Assess the morphology of the erythrocytes.
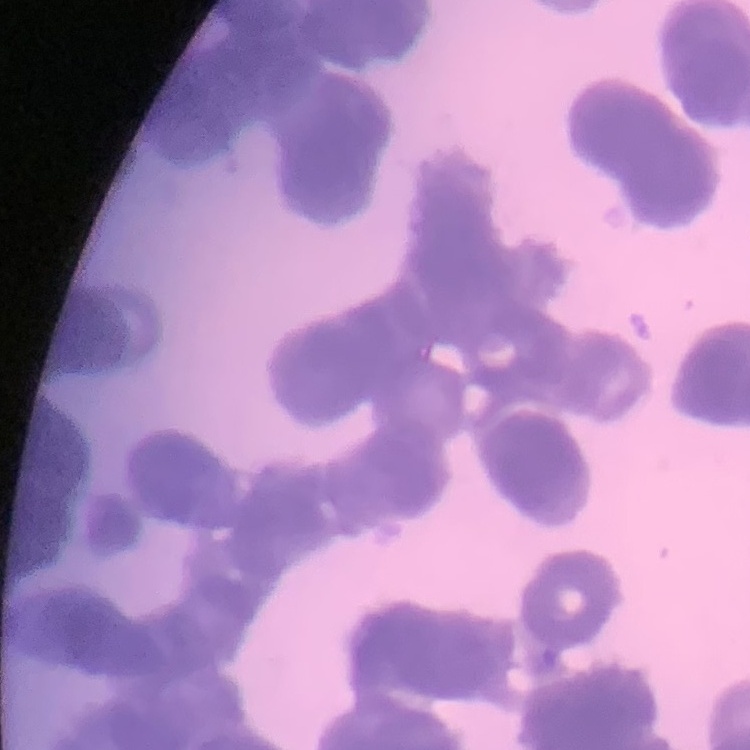
They show rouleaux formation.

Summary:
  - Image type: one tile cut from a larger photomicrograph
  - Stain: Field's or Giemsa
  - Preparation: thin blood smear